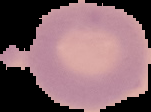
preparation: thin blood film
image_size: 151×112 pixels
result: negative for malaria parasites
image_type: segmented cell region on a black background